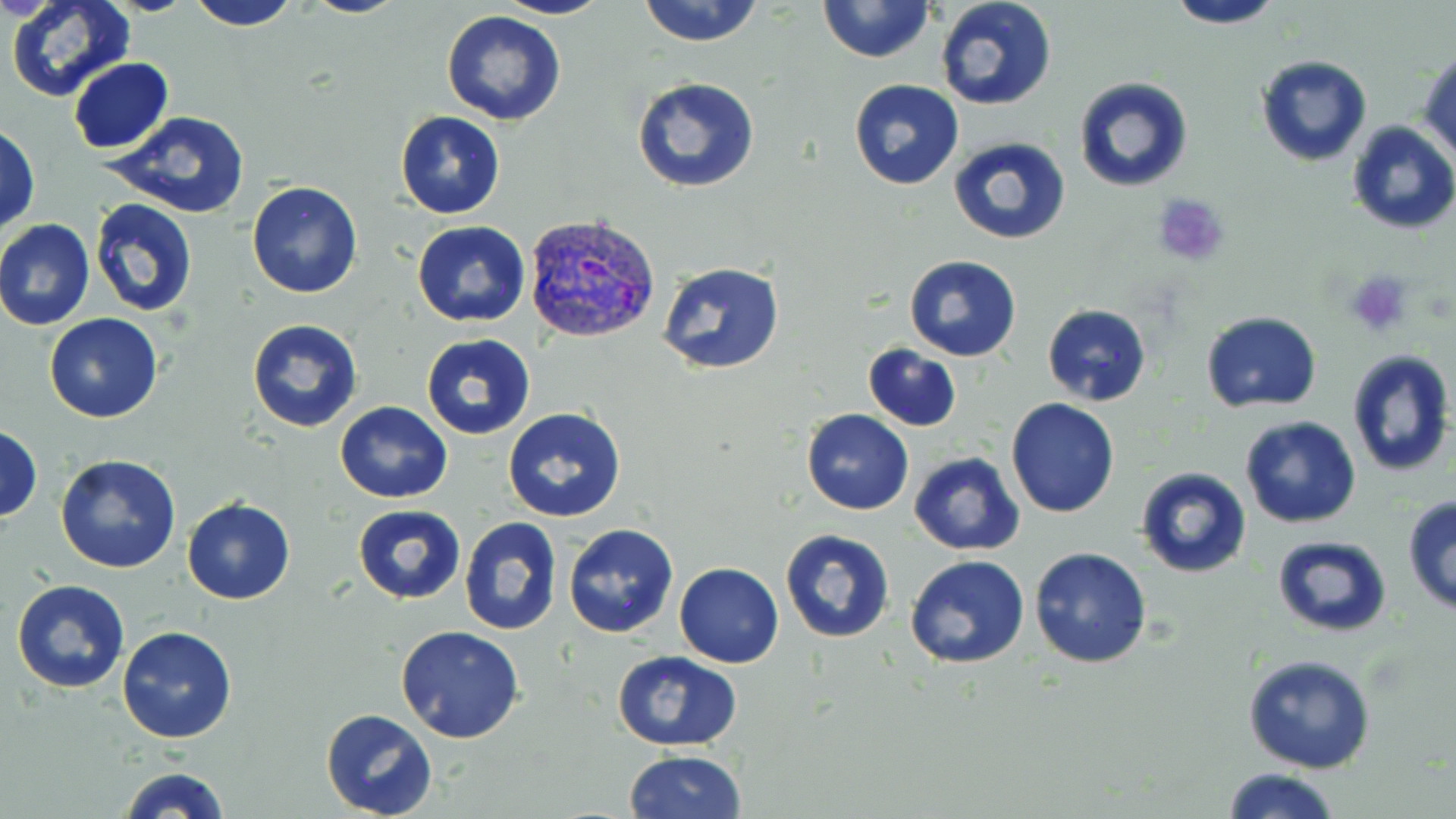 Approximate bounding boxes as (x1,y1)-(x2,y2) corner pairs in pixels. Plasmodium vivax-infected red blood cell locations: (525,212)-(659,343). Uninfected red blood cell locations: (6,0)-(133,103), (301,0)-(411,18), (495,0)-(609,21), (635,0)-(766,47), (819,0)-(934,63), (934,0)-(1057,111), (185,1)-(305,32), (1161,3)-(1288,30), (441,10)-(568,126), (1420,49)-(1455,161), (1256,56)-(1372,167), (68,57)-(175,154), (631,76)-(760,193), (1073,76)-(1194,192), (848,79)-(964,190), (104,111)-(252,220), (395,112)-(505,219), (1346,121)-(1456,234), (1,124)-(39,236), (948,137)-(1071,245), (247,180)-(363,299), (89,197)-(199,319), (0,217)-(96,330), (411,221)-(529,328), (904,255)-(1022,362), (658,262)-(784,377), (1042,303)-(1151,406), (1199,310)-(1323,415), (44,313)-(162,423), (246,319)-(363,433), (421,334)-(535,440), (862,343)-(962,433), (1346,349)-(1455,476), (1006,399)-(1120,518), (336,401)-(452,504), (503,406)-(626,523), (801,408)-(913,515), (1238,415)-(1361,529), (1,425)-(42,520), (909,451)-(1025,557), (55,454)-(181,574), (1135,468)-(1253,579), (1402,494)-(1456,619), (181,498)-(295,604), (352,504)-(465,603), (458,517)-(562,636), (564,522)-(678,639), (779,528)-(896,645), (1271,535)-(1391,637), (1028,546)-(1152,669), (904,555)-(1030,669), (674,562)-(784,668), (11,579)-(129,694), (395,626)-(525,745), (117,627)-(236,744), (610,650)-(743,751), (1242,654)-(1376,774), (320,709)-(437,819), (624,749)-(747,819), (118,765)-(231,819), (1219,767)-(1343,819). Platelet locations: (1149,190)-(1234,268), (1345,270)-(1414,337). Slide-level diagnosis: Plasmodium vivax. 1000x magnification. Optical microscopy. Single field of view. Thin blood smear. Image is 1456×819 pixels. May-Grünwald-Giemsa-stained preparation.